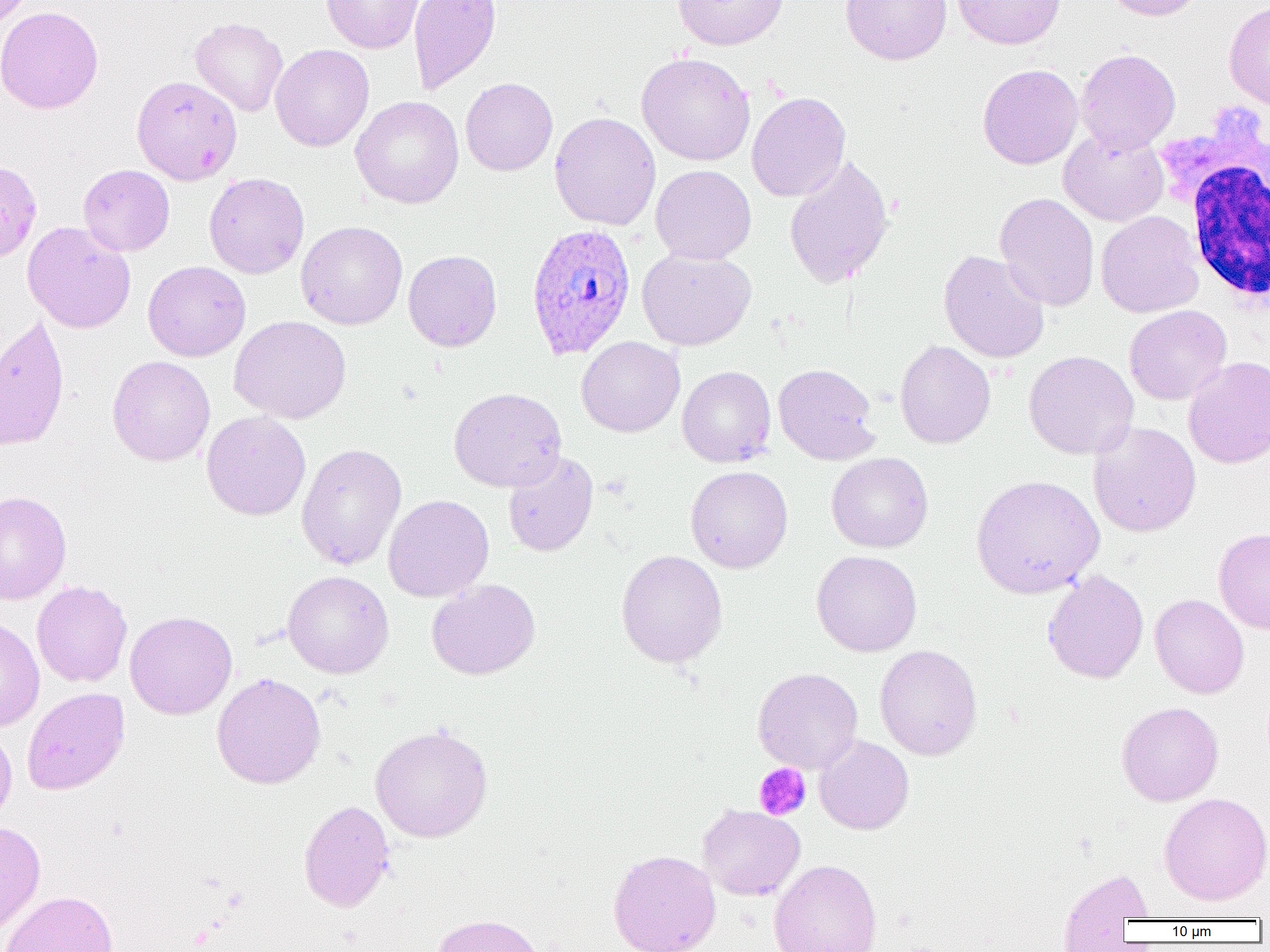

{
  "slide_level_diagnosis": "Plasmodium ovale",
  "preparation": "thin blood film",
  "white_blood_cell_locations": "approximate bounding boxes as [x1, y1, x2, y2] in pixels: [1165, 116, 1270, 310]",
  "plasmodium_ovale_infected_red_blood_cell_locations": "approximate bounding boxes as [x1, y1, x2, y2] in pixels: [526, 222, 637, 360]",
  "image_size": "1270×952 pixels",
  "field_of_view": "single",
  "modality": "optical microscopy",
  "magnification": "1000x",
  "platelet_locations": "approximate bounding boxes as [x1, y1, x2, y2] in pixels: [753, 763, 812, 821]",
  "uninfected_red_blood_cell_locations": "approximate bounding boxes as [x1, y1, x2, y2] in pixels: [0, 0, 35, 29], [322, 0, 424, 54], [408, 0, 501, 95], [672, 0, 790, 50], [840, 0, 951, 65], [952, 0, 1066, 50], [1103, 0, 1205, 21], [1223, 1, 1270, 111], [0, 5, 103, 114], [190, 17, 288, 117], [270, 44, 374, 152], [1076, 48, 1181, 155], [636, 52, 756, 166], [977, 64, 1083, 170], [132, 75, 242, 184], [460, 77, 558, 176], [747, 92, 851, 202], [350, 95, 464, 209], [549, 112, 661, 230], [1058, 127, 1169, 227], [783, 154, 894, 290], [0, 160, 42, 264], [78, 164, 175, 256], [651, 165, 756, 264], [203, 172, 309, 278], [995, 193, 1100, 311], [1096, 210, 1204, 318], [22, 221, 136, 333], [296, 221, 407, 330], [637, 248, 756, 350], [403, 250, 502, 352], [938, 250, 1050, 363], [143, 260, 251, 362], [1124, 305, 1232, 405], [0, 314, 70, 452], [229, 315, 351, 424], [577, 336, 685, 438], [894, 340, 996, 449], [1024, 350, 1138, 459], [107, 355, 215, 466], [1183, 356, 1270, 469], [773, 363, 881, 465], [677, 365, 776, 467], [448, 387, 566, 492], [201, 411, 311, 521], [1088, 421, 1201, 538], [296, 443, 407, 571], [502, 451, 598, 556], [826, 452, 934, 553], [686, 465, 793, 573], [971, 474, 1104, 599], [0, 490, 72, 605], [383, 494, 494, 602], [1213, 528, 1270, 634], [616, 549, 728, 668], [812, 550, 922, 656], [1042, 569, 1149, 684], [283, 571, 394, 678], [426, 578, 541, 680], [32, 580, 132, 688], [1149, 593, 1249, 698], [125, 611, 237, 719], [0, 614, 45, 732], [874, 644, 982, 760], [753, 667, 863, 774], [212, 672, 326, 789], [21, 687, 130, 795], [1116, 701, 1223, 806], [0, 722, 18, 826], [369, 723, 493, 842], [814, 736, 914, 835], [1159, 792, 1270, 906], [298, 800, 396, 912], [698, 804, 805, 901], [0, 820, 46, 939], [607, 850, 721, 952], [769, 859, 882, 952], [1056, 865, 1153, 950], [0, 890, 119, 952], [432, 913, 545, 952]"
}